Give the position of each Plasmodium falciparum parasite with its life-cycle stage, each leukocyte, and any debris.
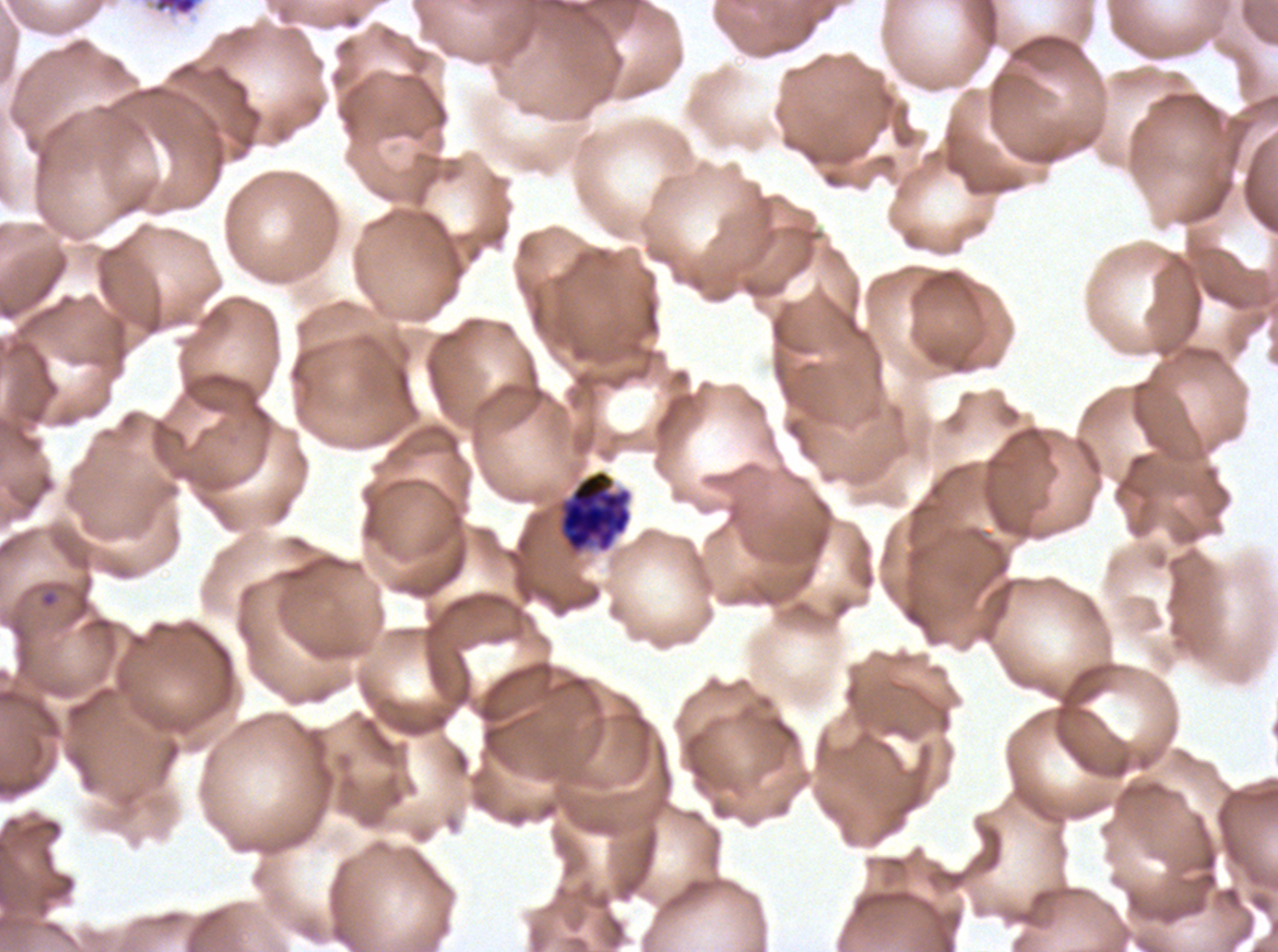
Approximate bounding rectangles given as corner coordinates in pixels from the top-left.
Rings: (x1=40, y1=589, x2=58, y2=608).
Late schizonts: (x1=154, y1=0, x2=200, y2=17).
Segmenters: (x1=558, y1=469, x2=633, y2=555).
No late-ring/early-trophozoite forms, mid trophozoites, late trophozoites, early schizonts, gametocytes, leukocytes, or debris observed.

preparation = thin blood film
life-cycle stages observed = ring, late schizont, segmenter
stain = Giemsa
image size = 1278×952 pixels
field of view = one sub-image of a larger composite
specimen = Plasmodium falciparum cultured ex vivo for 24 to 48 hours, from a patient in The Gambia